Assess the morphology of the red blood cells.
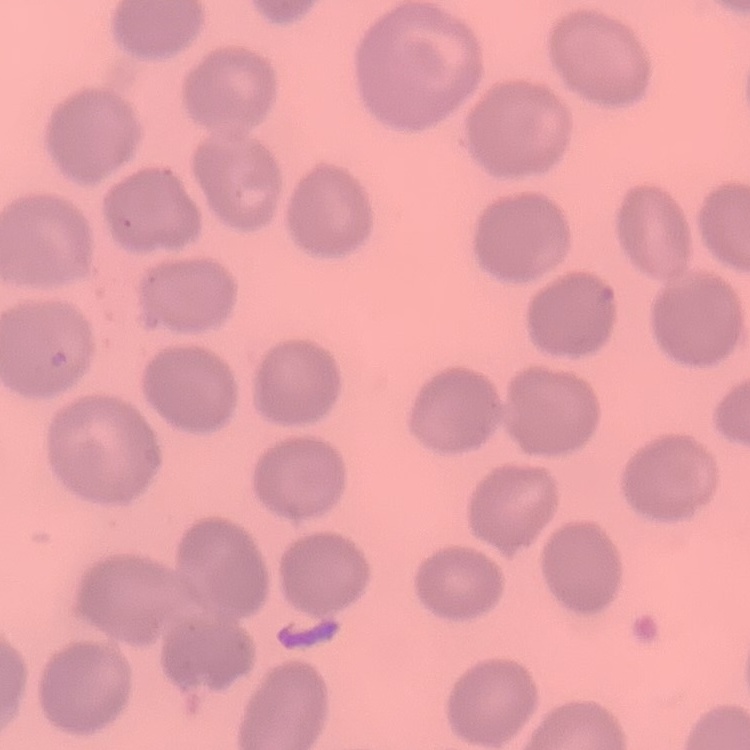

They show no rouleaux formation.

Thin blood film. Stained with either Field's or Giemsa. One tile cut from a larger photomicrograph.